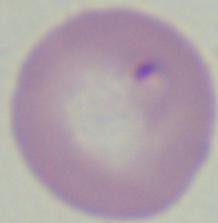
identification = Babesia
modality = micrograph
magnification = 1000x